Describe the morphology of the red blood cells.
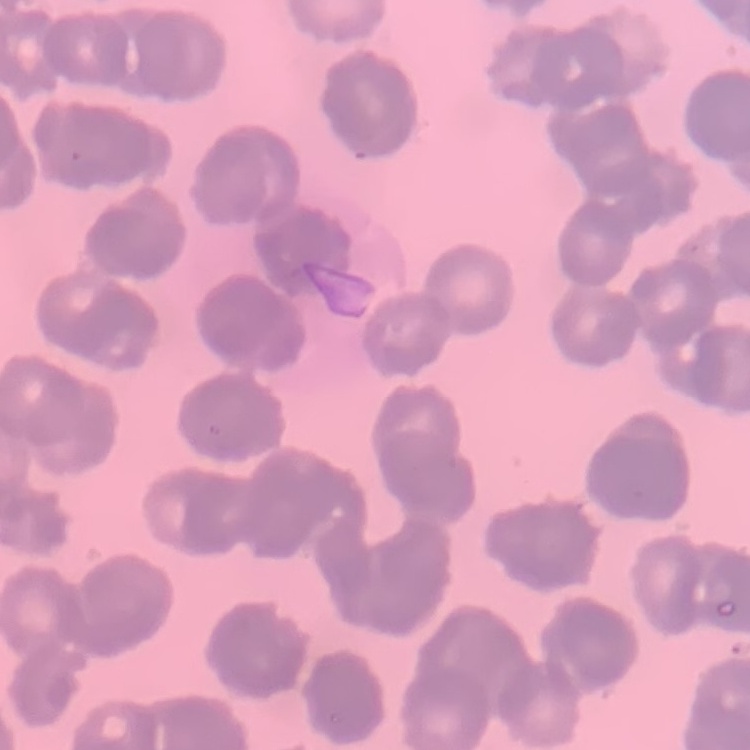
Rouleaux formation.

Summary:
  - Image type: square crop of a larger photomicrograph
  - Stain: Field's or Giemsa
  - Preparation: thin blood smear